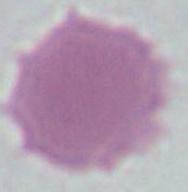
identification: erythrocyte
modality: micrograph
magnification: 1000x